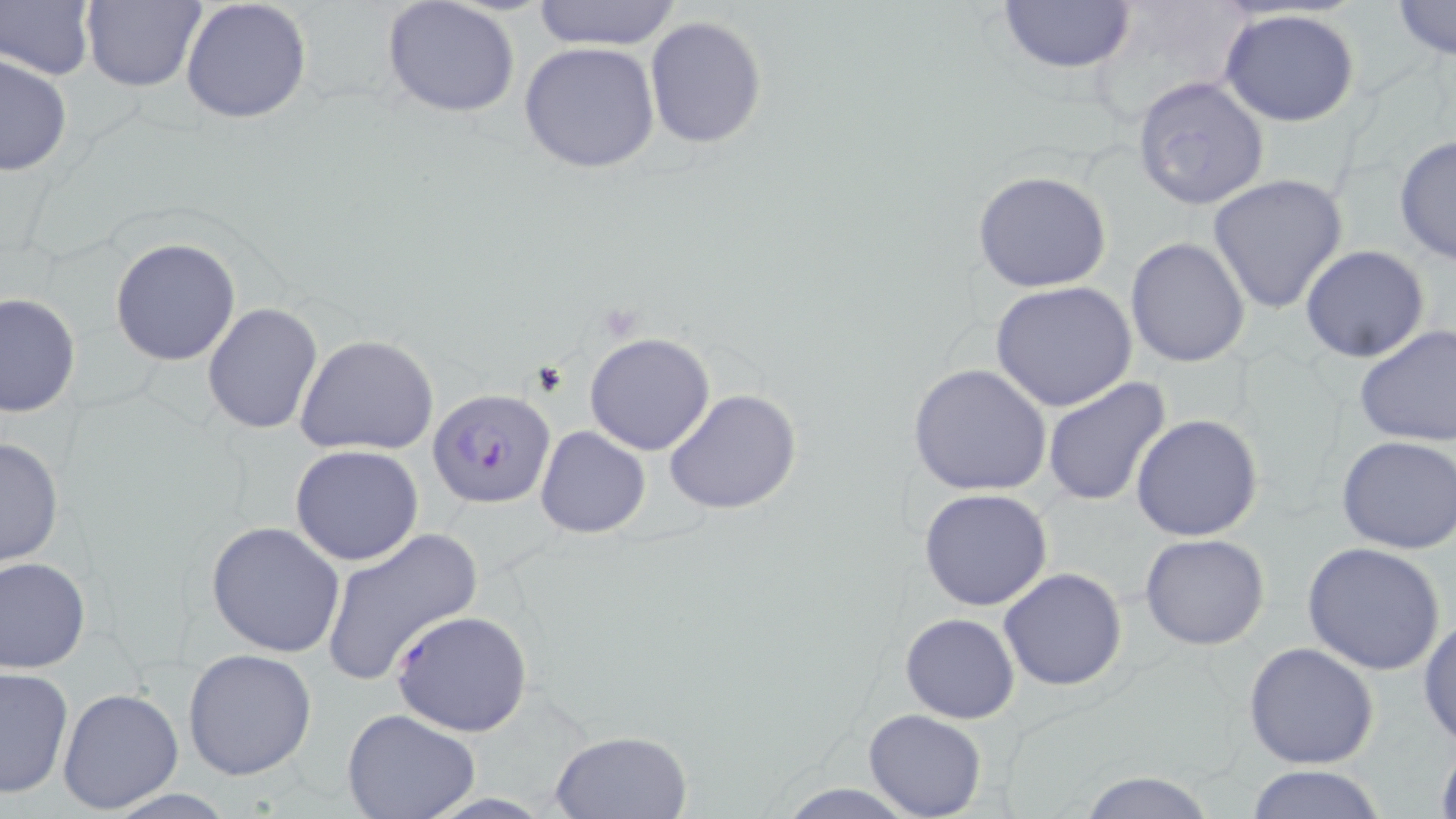

slide_level_diagnosis: Plasmodium falciparum
modality: light microscopy
magnification: 1000x
field_of_view: one of a larger specimen
stain: May-Grünwald-Giemsa
preparation: thin blood film
plasmodium_falciparum_infected_red_blood_cell_locations: 'approximate bounding boxes as (x1, y1, x2, y2) in pixels: (427, 388, 555, 508), (390, 609, 535, 737)'
uninfected_red_blood_cell_locations: 'approximate bounding boxes as (x1, y1, x2, y2) in pixels: (180, 0, 313, 123), (994, 0, 1138, 77), (81, 1, 205, 92), (381, 1, 521, 120), (528, 1, 686, 49), (1390, 1, 1455, 60), (2, 3, 94, 80), (1220, 9, 1362, 128), (643, 15, 770, 150), (519, 40, 662, 173), (0, 51, 74, 177), (1130, 74, 1269, 212), (1394, 135, 1456, 265), (971, 170, 1114, 293), (1207, 174, 1349, 314), (1125, 237, 1250, 369), (110, 238, 241, 365), (1301, 246, 1431, 363), (990, 281, 1138, 411), (0, 292, 80, 419), (203, 303, 324, 434), (1353, 323, 1456, 449), (584, 332, 716, 455), (293, 333, 439, 456), (909, 363, 1053, 498), (1041, 375, 1171, 505), (663, 386, 805, 516), (1130, 414, 1262, 542), (534, 425, 652, 538), (0, 435, 65, 569), (1336, 436, 1456, 555), (290, 445, 424, 566), (918, 488, 1053, 612), (205, 521, 345, 658), (319, 528, 484, 687), (1139, 533, 1270, 650), (1302, 540, 1445, 674), (0, 556, 91, 673), (998, 568, 1128, 692), (900, 612, 1020, 723), (1418, 613, 1456, 749), (1243, 641, 1379, 769), (182, 648, 317, 780), (1, 666, 73, 798), (57, 687, 184, 814), (865, 709, 986, 819), (342, 710, 479, 819), (549, 729, 694, 817), (1433, 735, 1456, 819), (1242, 765, 1388, 819), (1073, 770, 1223, 819), (773, 782, 922, 817)'
image_size: 1456×819 pixels